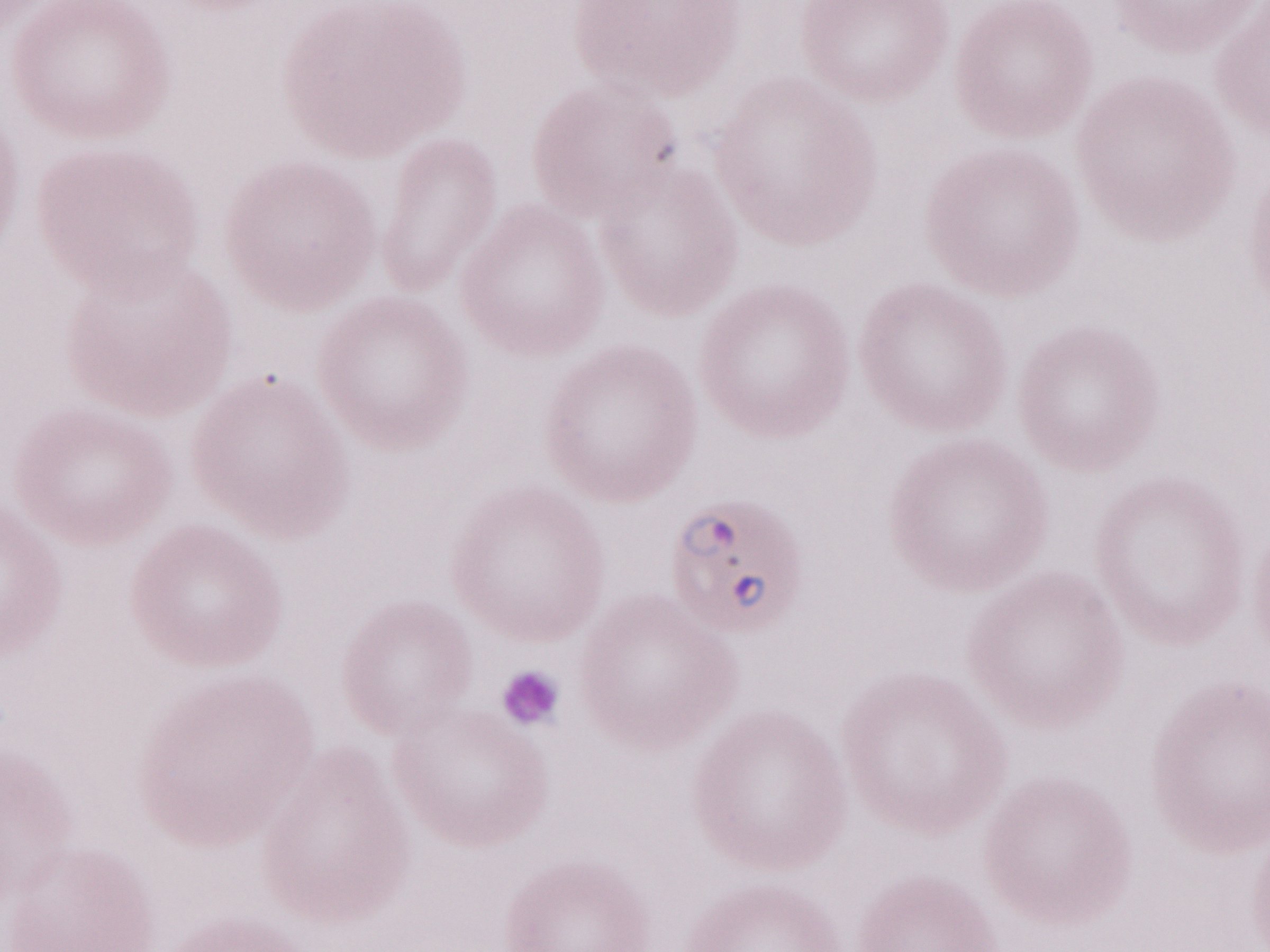

Thin blood smear. Single field of view. Olympus BX43 microscope, Olympus DP73 camera. 1,000x magnification. Malaria diagnosis (patient-level): positive. Image is 1270×952 pixels. May-Grünwald-Giemsa-stained preparation.